Locate every white blood cell.
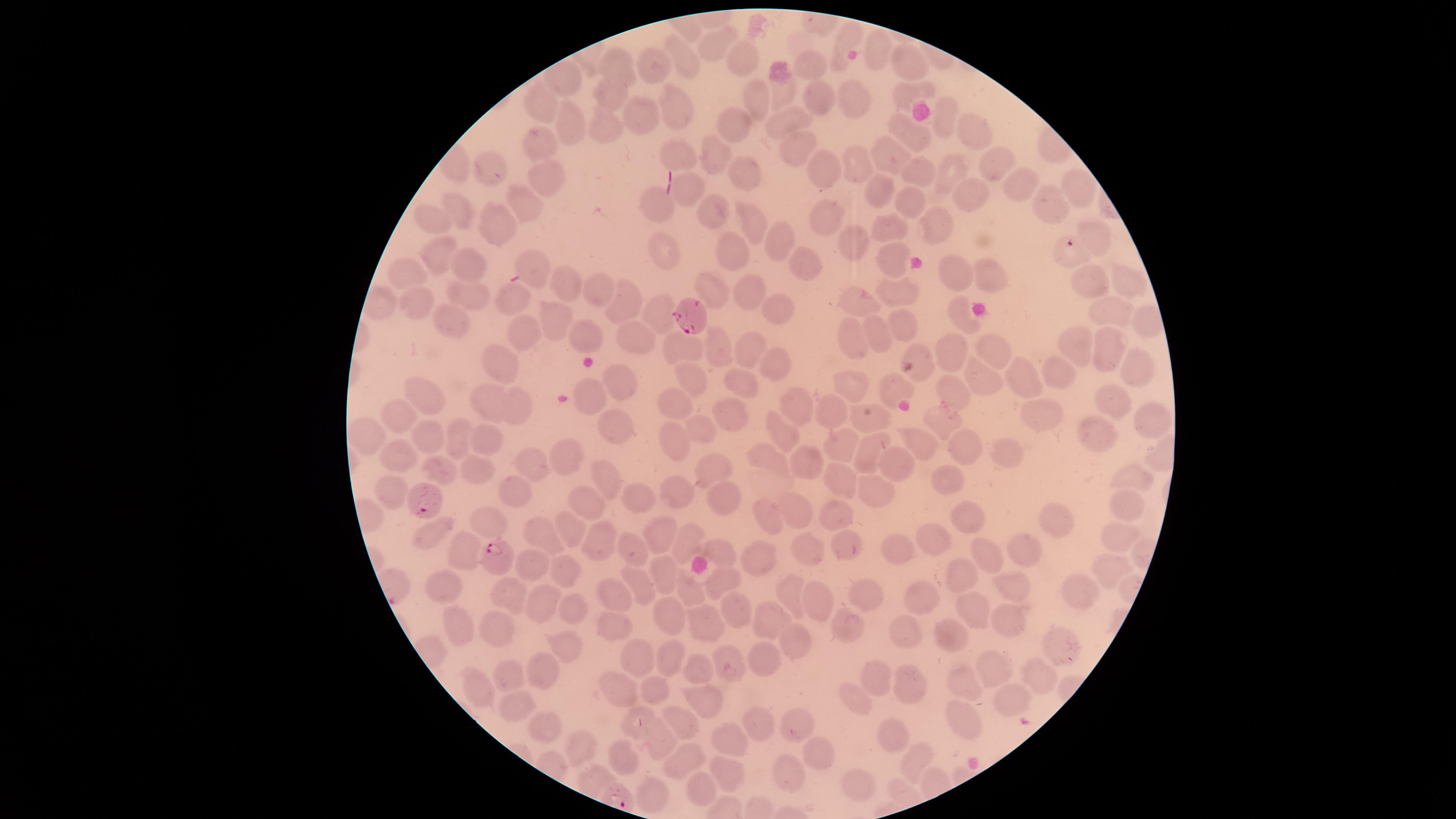

No white blood cells identified.

Approximate marker points as [x, y] in pixels. Uninfected red blood cells: [849, 36], [718, 44], [877, 45], [681, 56], [738, 61], [622, 62], [907, 62], [654, 64], [809, 66], [565, 79], [610, 93], [902, 93], [781, 94], [757, 98], [817, 98], [852, 98], [675, 105], [543, 107], [646, 116], [944, 116], [790, 119], [733, 123], [569, 129], [606, 130], [908, 131], [974, 131], [793, 140], [537, 144], [680, 154], [715, 154], [890, 156], [996, 160], [856, 161], [488, 163], [820, 167], [740, 171], [918, 172], [948, 173], [547, 175], [1013, 182], [1077, 185], [879, 190], [689, 191], [967, 196], [659, 201], [909, 202], [1044, 202], [523, 204], [461, 212], [712, 212], [824, 214], [428, 218], [748, 218], [890, 224], [937, 226], [500, 227], [1093, 233], [781, 239], [857, 243], [437, 252], [665, 254], [893, 256], [736, 257], [538, 265], [802, 265], [468, 269], [410, 271], [955, 272], [991, 276], [1081, 280], [567, 285], [1129, 285], [709, 286], [596, 288], [744, 290], [469, 292], [896, 293], [519, 295], [415, 298], [623, 304], [858, 305], [779, 307], [660, 308], [1110, 310], [550, 317], [961, 317], [1143, 319], [446, 322], [908, 324], [875, 333], [527, 335], [587, 336], [637, 338], [848, 340], [1106, 342], [1073, 343], [713, 346], [751, 346], [677, 347], [948, 347], [985, 347], [775, 358], [1138, 360], [505, 362], [978, 374], [1060, 374], [693, 377], [617, 381], [740, 381], [1023, 381], [848, 385], [897, 386], [950, 387], [590, 392], [1110, 394], [426, 395], [485, 401], [677, 402], [794, 403], [519, 409], [829, 410], [730, 411], [1048, 415], [395, 417], [942, 417], [616, 421], [869, 423], [699, 424], [1153, 425], [778, 428], [1100, 431], [429, 434], [460, 434], [368, 435], [672, 435], [491, 443], [967, 443], [928, 444], [832, 446], [870, 450], [565, 454], [1011, 456], [805, 457], [401, 458], [773, 458], [534, 462], [900, 463], [708, 466], [438, 469], [481, 473], [609, 476], [947, 477], [840, 478], [1134, 480], [392, 487], [512, 489], [878, 489], [677, 491], [716, 492], [637, 499], [582, 502], [1122, 502], [789, 510], [764, 514], [830, 518], [971, 520], [480, 521], [1057, 523], [569, 529], [664, 533], [433, 535], [543, 536], [939, 537], [1120, 537], [603, 542], [688, 543], [639, 546], [900, 547], [804, 550], [721, 552], [1028, 554], [466, 555], [982, 556], [764, 560], [534, 565], [1108, 568], [561, 571], [956, 572], [663, 573], [635, 576], [724, 581], [449, 586], [792, 588], [1005, 588], [1080, 589], [689, 592], [867, 592], [508, 596], [619, 598], [919, 598], [820, 601], [537, 602], [730, 606], [576, 607], [971, 608], [668, 615], [769, 620], [1008, 620], [841, 622], [708, 626], [495, 629], [616, 629], [462, 632], [946, 636], [915, 637], [799, 643], [569, 651], [1054, 652], [668, 658], [634, 660], [766, 663], [703, 665], [728, 668], [999, 671], [514, 673], [547, 673], [1035, 674], [878, 683], [908, 683], [662, 685], [972, 685], [481, 687], [616, 689], [703, 696], [1009, 701], [862, 702], [513, 709], [755, 720], [797, 723], [966, 723], [685, 724], [544, 725], [888, 735], [662, 738], [581, 742], [729, 745], [821, 756], [622, 760], [684, 760], [917, 761], [724, 768], [789, 771], [592, 783], [863, 785], [701, 789], [652, 792]. Parasitized red blood cells: [1069, 250], [693, 316], [425, 497], [494, 559]. Single field of view. Species: Plasmodium falciparum. Thin blood film. Circular visible region. Presence: malaria parasites detected. Photographed with a smartphone camera through the microscope eyepiece. Giemsa stain. Image is 1456×819 pixels.